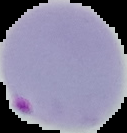
image type = segmented cell region on a black background
malaria status = parasitized
image size = 127×133 pixels
preparation = thin blood smear